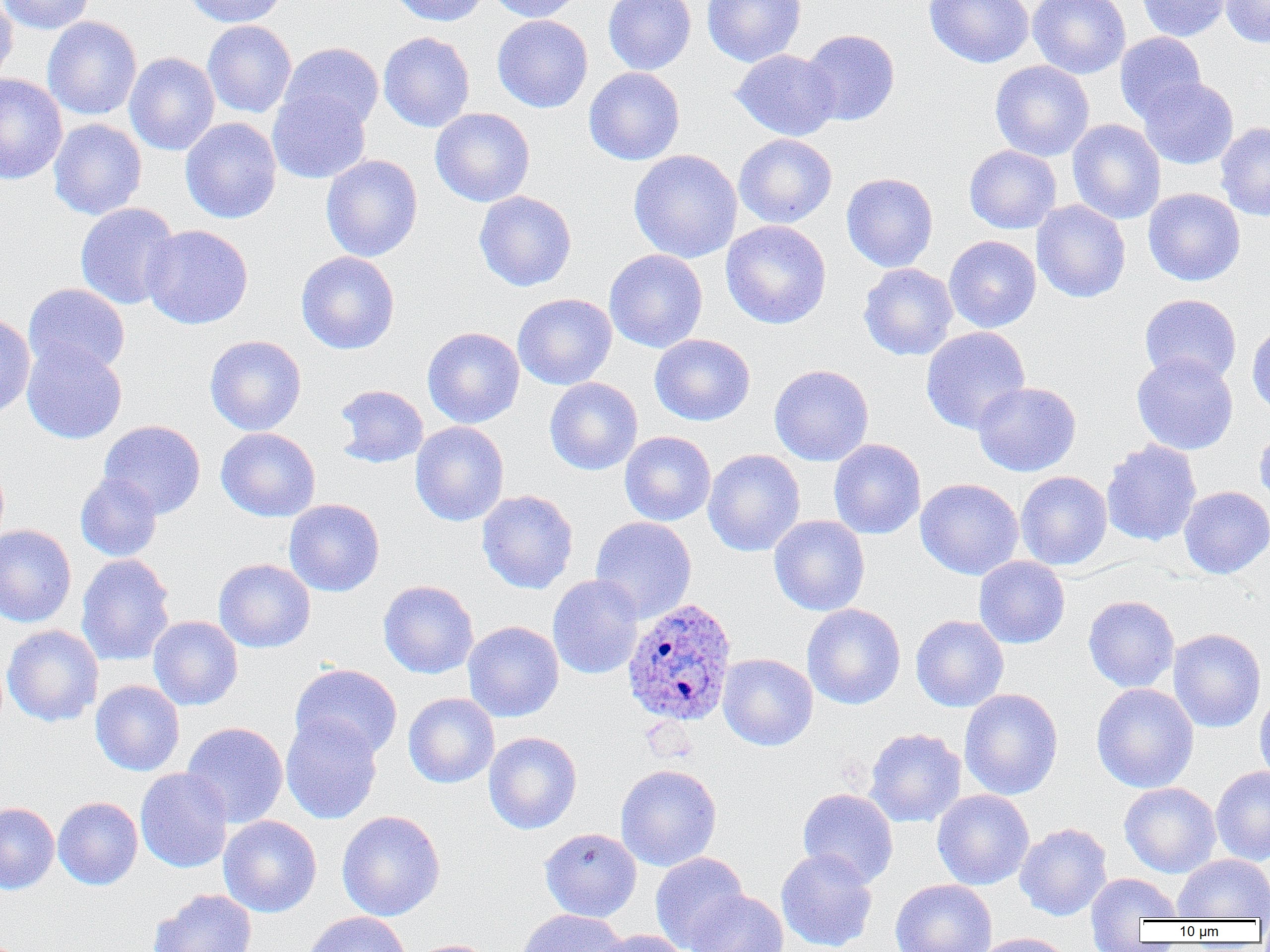
Plasmodium ovale-infected red blood cell locations = approximate bounding boxes as named x1/y1/x2/y2 corners in pixels: (x1=622, y1=597, x2=738, y2=726)
slide-level diagnosis = Plasmodium ovale
modality = optical microscopy
field of view = one of a larger specimen
magnification = 1000x
preparation = thin blood smear
image size = 1270×952 pixels
uninfected red blood cell locations = approximate bounding boxes as named x1/y1/x2/y2 corners in pixels: (x1=0, y1=0, x2=95, y2=35), (x1=0, y1=0, x2=18, y2=86), (x1=184, y1=0, x2=288, y2=27), (x1=388, y1=0, x2=487, y2=27), (x1=486, y1=0, x2=584, y2=22), (x1=603, y1=0, x2=696, y2=75), (x1=702, y1=0, x2=806, y2=66), (x1=924, y1=0, x2=1035, y2=67), (x1=1027, y1=0, x2=1130, y2=79), (x1=1135, y1=0, x2=1232, y2=41), (x1=1220, y1=0, x2=1270, y2=48), (x1=492, y1=15, x2=593, y2=112), (x1=42, y1=16, x2=142, y2=120), (x1=202, y1=20, x2=297, y2=118), (x1=801, y1=29, x2=900, y2=126), (x1=378, y1=32, x2=475, y2=132), (x1=1115, y1=32, x2=1206, y2=123), (x1=278, y1=43, x2=383, y2=135), (x1=731, y1=49, x2=839, y2=141), (x1=124, y1=52, x2=220, y2=155), (x1=990, y1=60, x2=1094, y2=161), (x1=583, y1=67, x2=685, y2=166), (x1=0, y1=74, x2=68, y2=185), (x1=1138, y1=77, x2=1238, y2=169), (x1=267, y1=86, x2=371, y2=184), (x1=430, y1=107, x2=535, y2=207), (x1=180, y1=117, x2=282, y2=224), (x1=49, y1=118, x2=147, y2=219), (x1=1067, y1=119, x2=1166, y2=224), (x1=1215, y1=122, x2=1270, y2=221), (x1=734, y1=134, x2=837, y2=228), (x1=964, y1=145, x2=1061, y2=234), (x1=628, y1=149, x2=742, y2=263), (x1=321, y1=154, x2=422, y2=262), (x1=841, y1=172, x2=938, y2=272), (x1=1143, y1=188, x2=1245, y2=286), (x1=474, y1=190, x2=577, y2=291), (x1=1032, y1=200, x2=1130, y2=303), (x1=75, y1=202, x2=181, y2=310), (x1=721, y1=220, x2=831, y2=329), (x1=140, y1=224, x2=253, y2=330), (x1=944, y1=235, x2=1041, y2=332), (x1=604, y1=249, x2=708, y2=353), (x1=296, y1=251, x2=400, y2=354), (x1=859, y1=263, x2=958, y2=361), (x1=23, y1=283, x2=130, y2=377), (x1=512, y1=293, x2=617, y2=389), (x1=1139, y1=294, x2=1241, y2=385), (x1=0, y1=314, x2=35, y2=418), (x1=1247, y1=320, x2=1270, y2=417), (x1=423, y1=326, x2=525, y2=428), (x1=921, y1=326, x2=1030, y2=434), (x1=649, y1=334, x2=755, y2=426), (x1=204, y1=335, x2=307, y2=436), (x1=22, y1=341, x2=127, y2=444), (x1=1131, y1=353, x2=1238, y2=455), (x1=769, y1=364, x2=874, y2=466), (x1=545, y1=377, x2=643, y2=475), (x1=972, y1=381, x2=1081, y2=476), (x1=333, y1=384, x2=429, y2=468), (x1=98, y1=420, x2=206, y2=519), (x1=410, y1=421, x2=509, y2=526), (x1=1253, y1=423, x2=1270, y2=512), (x1=216, y1=427, x2=321, y2=521), (x1=619, y1=431, x2=716, y2=526), (x1=828, y1=438, x2=925, y2=539), (x1=1101, y1=439, x2=1202, y2=546), (x1=703, y1=449, x2=805, y2=557), (x1=1015, y1=471, x2=1112, y2=570), (x1=75, y1=472, x2=163, y2=562), (x1=915, y1=478, x2=1024, y2=580), (x1=1179, y1=486, x2=1270, y2=579), (x1=477, y1=490, x2=578, y2=594), (x1=284, y1=499, x2=385, y2=597), (x1=769, y1=515, x2=870, y2=616), (x1=590, y1=516, x2=697, y2=623), (x1=0, y1=524, x2=77, y2=628), (x1=76, y1=553, x2=175, y2=666), (x1=974, y1=556, x2=1070, y2=649), (x1=213, y1=558, x2=316, y2=653), (x1=547, y1=575, x2=644, y2=680), (x1=378, y1=580, x2=479, y2=679), (x1=1083, y1=595, x2=1179, y2=692), (x1=802, y1=604, x2=905, y2=710), (x1=910, y1=614, x2=1009, y2=712), (x1=148, y1=616, x2=243, y2=710), (x1=463, y1=621, x2=564, y2=722), (x1=2, y1=624, x2=104, y2=727), (x1=1167, y1=628, x2=1266, y2=733), (x1=718, y1=653, x2=818, y2=751), (x1=290, y1=663, x2=403, y2=760), (x1=90, y1=680, x2=184, y2=776), (x1=1254, y1=682, x2=1270, y2=788), (x1=1091, y1=683, x2=1199, y2=793), (x1=959, y1=688, x2=1063, y2=800), (x1=403, y1=692, x2=500, y2=788), (x1=281, y1=714, x2=382, y2=824), (x1=181, y1=721, x2=289, y2=828), (x1=864, y1=728, x2=966, y2=828), (x1=483, y1=731, x2=582, y2=834), (x1=616, y1=763, x2=722, y2=871), (x1=1210, y1=765, x2=1270, y2=865), (x1=135, y1=768, x2=233, y2=873), (x1=1119, y1=782, x2=1221, y2=878), (x1=797, y1=788, x2=898, y2=888), (x1=932, y1=789, x2=1034, y2=890), (x1=53, y1=796, x2=143, y2=890), (x1=0, y1=802, x2=59, y2=894), (x1=336, y1=810, x2=445, y2=921), (x1=218, y1=815, x2=322, y2=917), (x1=1014, y1=823, x2=1112, y2=921), (x1=540, y1=827, x2=641, y2=922), (x1=776, y1=848, x2=878, y2=952), (x1=650, y1=852, x2=749, y2=951), (x1=1173, y1=854, x2=1270, y2=920), (x1=1085, y1=872, x2=1182, y2=942), (x1=890, y1=879, x2=997, y2=952), (x1=148, y1=888, x2=257, y2=952), (x1=686, y1=889, x2=789, y2=952), (x1=517, y1=908, x2=627, y2=952), (x1=301, y1=912, x2=411, y2=952), (x1=594, y1=929, x2=689, y2=952), (x1=973, y1=933, x2=1072, y2=952), (x1=408, y1=939, x2=501, y2=952)